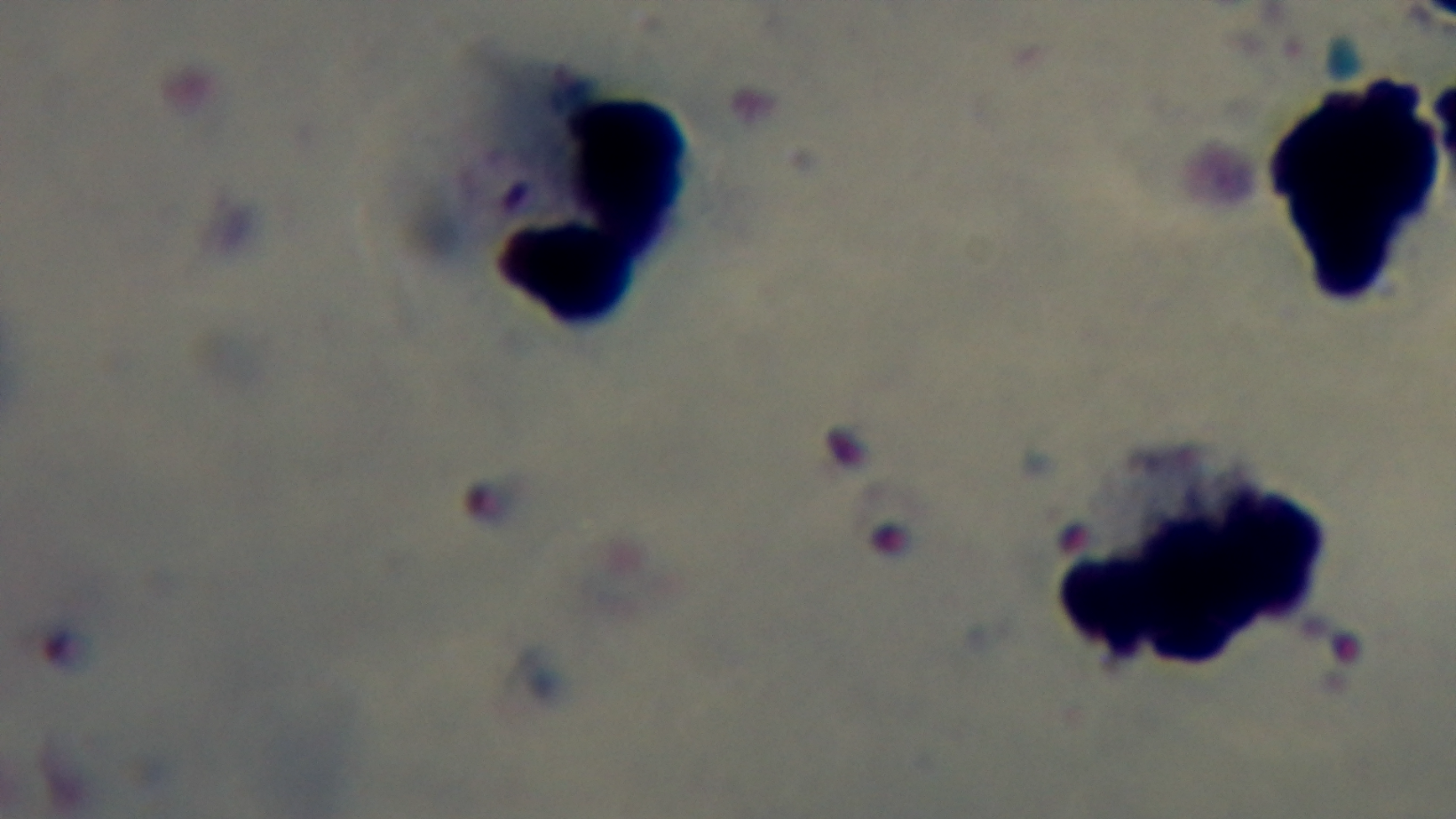

modality = light microscopy
objective = 100x oil immersion
preparation = thick blood film
malaria status = infected
capture = mounted 4K digital camera
stain = Giemsa
field of view = single